Name the parasite shown.
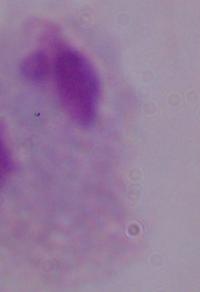
A trichomonad.

Photomicrograph. 1000x magnification.